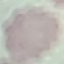
Summary:
  - Result: negative for malaria parasites
  - Stain: Giemsa
  - Preparation: thin blood smear
  - Image type: cell patch, automatically extracted from a larger field of view and resized to 64 × 64 pixels
  - Capture: smartphone camera at the microscope eyepiece